Give the position of every Plasmodium parasite.
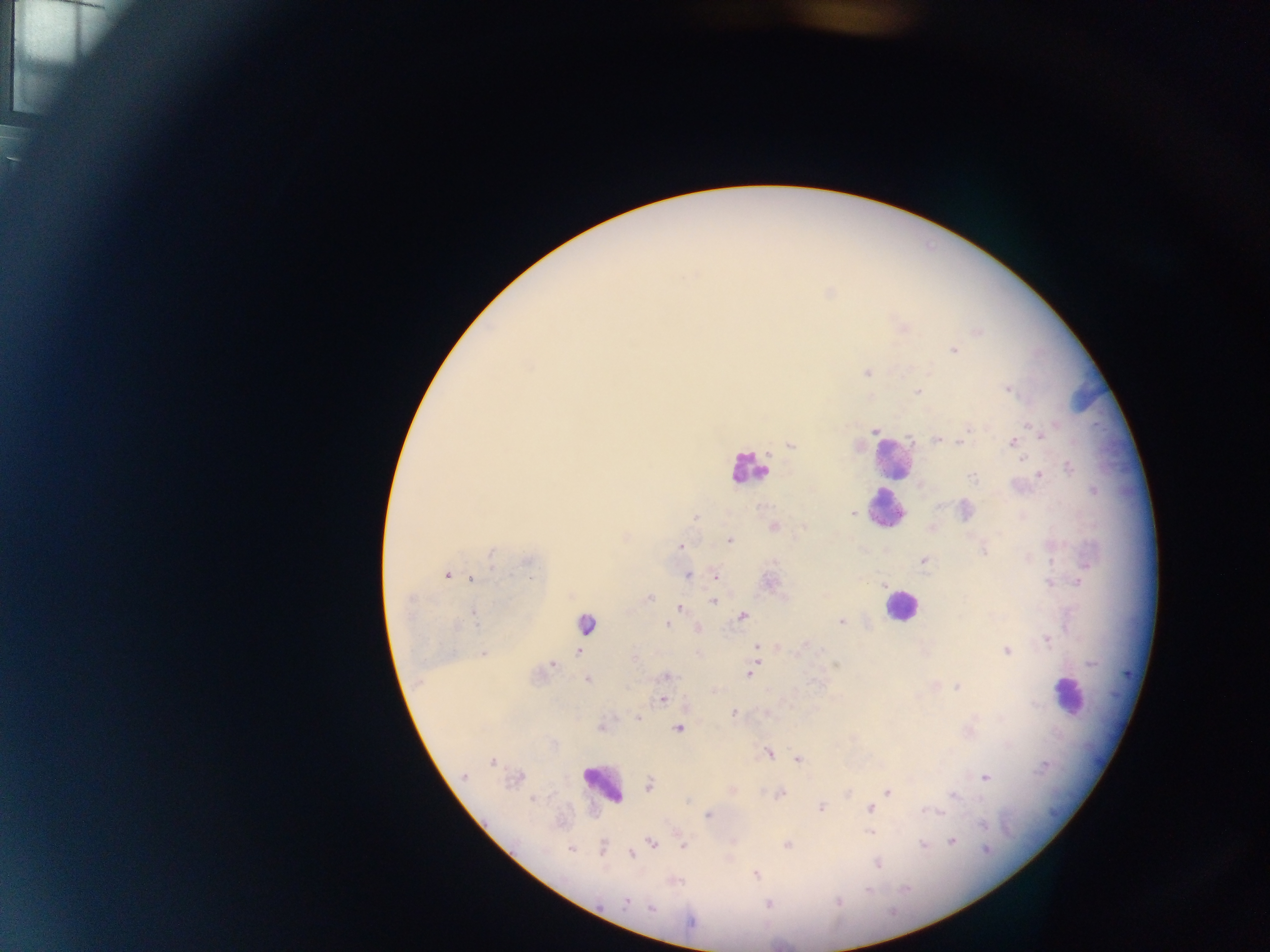
Approximate centers as {x, y} in pixels.
Plasmodium parasites: {978, 332}, {954, 351}, {867, 373}, {1008, 390}, {917, 391}, {971, 428}, {875, 431}, {1039, 433}, {966, 434}, {936, 439}, {961, 442}, {1013, 442}, {791, 445}, {1070, 467}, {1039, 475}, {972, 477}, {852, 513}, {696, 516}, {774, 526}, {730, 540}, {681, 546}, {984, 550}, {491, 552}, {529, 561}, {924, 561}, {447, 574}, {688, 575}, {715, 575}, {472, 579}, {1079, 583}, {883, 585}, {650, 598}, {712, 601}, {680, 608}, {474, 612}, {743, 616}, {842, 621}, {585, 623}, {667, 625}, {456, 626}, {1047, 640}, {756, 647}, {578, 651}, {1006, 651}, {483, 653}, {758, 660}, {553, 665}, {836, 666}, {749, 674}, {667, 676}, {587, 681}, {957, 687}, {663, 700}, {733, 713}, {637, 719}, {679, 728}, {768, 753}, {797, 760}, {492, 762}, {464, 776}, {985, 778}, {650, 785}, {888, 792}, {780, 794}, {954, 796}, {532, 799}, {686, 802}, {873, 804}, {821, 808}, {870, 808}, {928, 811}, {708, 815}, {983, 824}, {869, 831}, {952, 842}, {652, 843}, {922, 844}, {787, 845}, {682, 846}, {571, 848}, {602, 848}, {986, 849}, {631, 854}, {878, 864}, {757, 875}, {869, 890}, {626, 902}, {651, 908}, {691, 921}.

Leukocyte locations: {892, 457}, {748, 469}, {886, 510}, {901, 605}, {1067, 695}, {602, 784}. Thick blood smear. Photographed through a microscope with a mobile-phone camera. Image is 1270×952 pixels. Single field of view. Collected in Ghana.